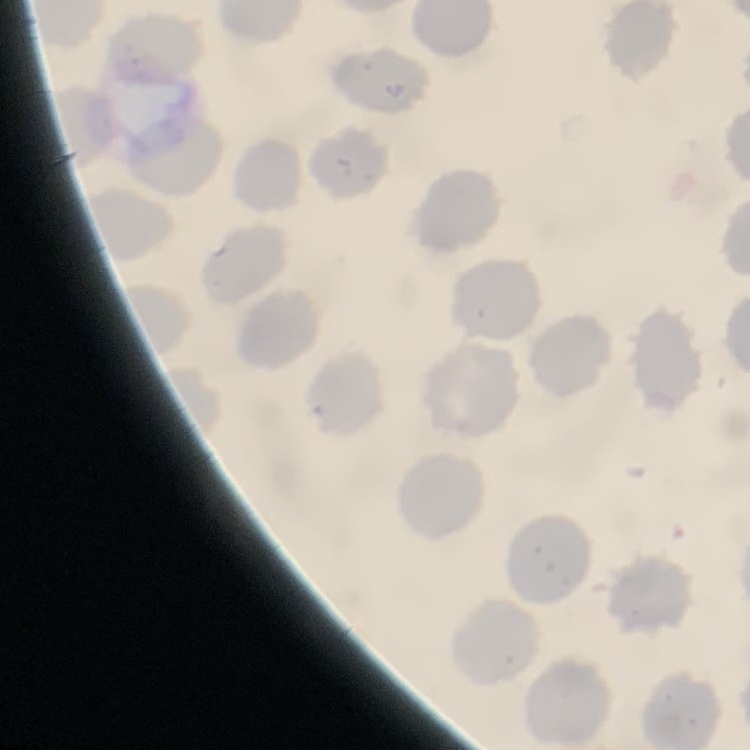
Summary:
  - Erythrocyte morphology: no rouleaux formation
  - Image type: square crop of a larger photomicrograph
  - Preparation: thin blood smear
  - Stain: Field's or Giemsa